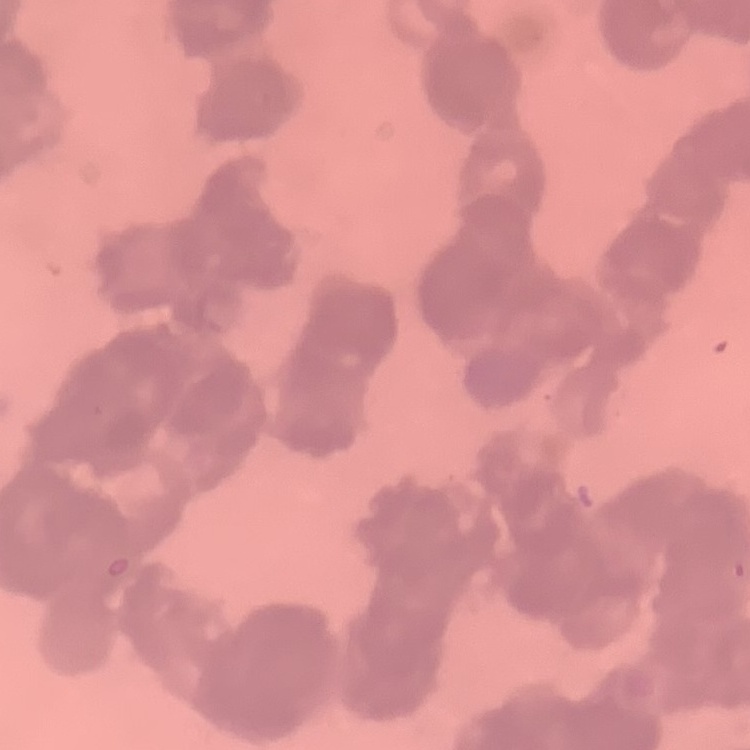
erythrocyte morphology = rouleaux formation
stain = Field's or Giemsa
preparation = thin blood film
image type = square crop of a larger photomicrograph